Name the blood parasite species.
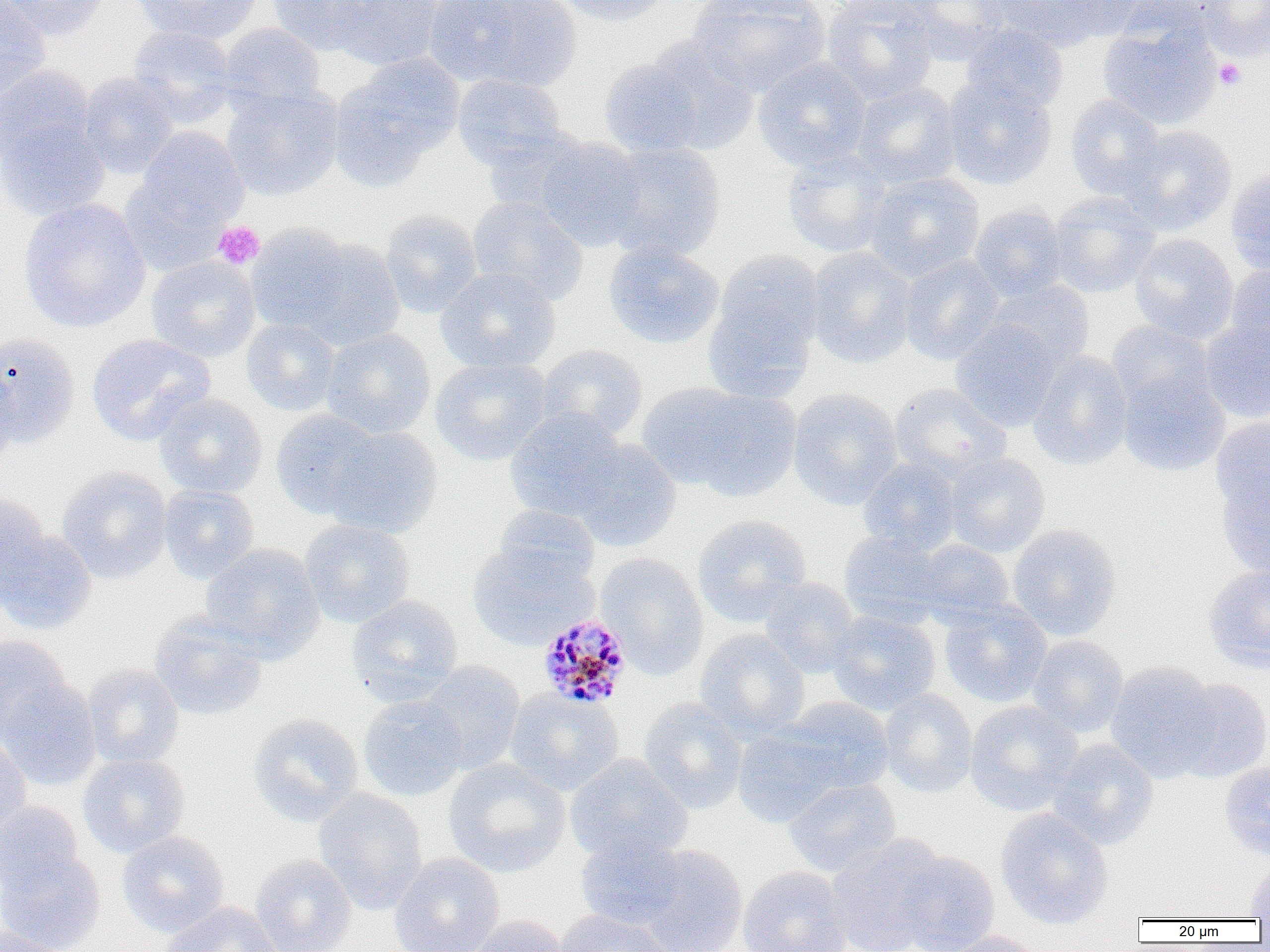

Plasmodium malariae.

Approximate bounding boxes as named x1/y1/x2/y2 corners in pixels. Uninfected red blood cell locations: (x1=0, y1=0, x2=50, y2=99), (x1=3, y1=0, x2=110, y2=39), (x1=134, y1=0, x2=263, y2=44), (x1=268, y1=0, x2=382, y2=55), (x1=328, y1=0, x2=444, y2=72), (x1=433, y1=0, x2=581, y2=92), (x1=553, y1=0, x2=671, y2=26), (x1=687, y1=0, x2=830, y2=96), (x1=822, y1=0, x2=940, y2=105), (x1=899, y1=0, x2=1014, y2=65), (x1=986, y1=0, x2=1127, y2=50), (x1=1044, y1=0, x2=1157, y2=40), (x1=1195, y1=0, x2=1270, y2=61), (x1=1099, y1=19, x2=1222, y2=130), (x1=217, y1=23, x2=327, y2=117), (x1=960, y1=24, x2=1068, y2=116), (x1=127, y1=26, x2=237, y2=129), (x1=643, y1=37, x2=759, y2=155), (x1=598, y1=56, x2=707, y2=157), (x1=752, y1=56, x2=872, y2=172), (x1=332, y1=58, x2=462, y2=186), (x1=0, y1=64, x2=95, y2=163), (x1=78, y1=72, x2=179, y2=179), (x1=453, y1=73, x2=567, y2=169), (x1=942, y1=77, x2=1058, y2=191), (x1=848, y1=82, x2=961, y2=188), (x1=221, y1=86, x2=344, y2=200), (x1=1065, y1=94, x2=1167, y2=201), (x1=0, y1=117, x2=110, y2=220), (x1=1118, y1=124, x2=1237, y2=235), (x1=135, y1=127, x2=250, y2=232), (x1=483, y1=128, x2=591, y2=220), (x1=534, y1=137, x2=646, y2=251), (x1=600, y1=141, x2=727, y2=262), (x1=782, y1=147, x2=896, y2=259), (x1=1225, y1=170, x2=1270, y2=275), (x1=864, y1=172, x2=985, y2=282), (x1=1047, y1=193, x2=1161, y2=297), (x1=467, y1=196, x2=588, y2=306), (x1=18, y1=198, x2=151, y2=333), (x1=969, y1=203, x2=1067, y2=301), (x1=381, y1=209, x2=482, y2=318), (x1=246, y1=223, x2=356, y2=335), (x1=1129, y1=233, x2=1239, y2=344), (x1=294, y1=237, x2=405, y2=350), (x1=603, y1=241, x2=724, y2=349), (x1=806, y1=246, x2=917, y2=369), (x1=703, y1=251, x2=824, y2=399), (x1=899, y1=254, x2=1005, y2=365), (x1=145, y1=256, x2=260, y2=362), (x1=1225, y1=263, x2=1270, y2=367), (x1=436, y1=267, x2=561, y2=374), (x1=986, y1=278, x2=1095, y2=372), (x1=242, y1=319, x2=341, y2=416), (x1=1201, y1=319, x2=1270, y2=423), (x1=950, y1=320, x2=1060, y2=432), (x1=1107, y1=321, x2=1217, y2=418), (x1=321, y1=328, x2=436, y2=440), (x1=0, y1=333, x2=80, y2=448), (x1=86, y1=333, x2=215, y2=445), (x1=536, y1=345, x2=648, y2=443), (x1=1028, y1=351, x2=1134, y2=471), (x1=430, y1=356, x2=552, y2=466), (x1=0, y1=364, x2=18, y2=470), (x1=1117, y1=369, x2=1231, y2=477), (x1=890, y1=383, x2=1011, y2=482), (x1=647, y1=385, x2=802, y2=500), (x1=787, y1=387, x2=903, y2=509), (x1=154, y1=392, x2=268, y2=499), (x1=503, y1=408, x2=627, y2=522), (x1=270, y1=409, x2=384, y2=520), (x1=1210, y1=417, x2=1270, y2=520), (x1=321, y1=425, x2=442, y2=538), (x1=568, y1=438, x2=682, y2=552), (x1=942, y1=453, x2=1051, y2=557), (x1=858, y1=458, x2=961, y2=556), (x1=56, y1=466, x2=172, y2=583), (x1=1215, y1=469, x2=1270, y2=577), (x1=159, y1=485, x2=259, y2=584), (x1=0, y1=495, x2=54, y2=601), (x1=492, y1=503, x2=600, y2=589), (x1=693, y1=513, x2=812, y2=627), (x1=299, y1=519, x2=416, y2=627), (x1=1006, y1=524, x2=1122, y2=641), (x1=0, y1=527, x2=97, y2=634), (x1=839, y1=530, x2=949, y2=627), (x1=910, y1=538, x2=1015, y2=627), (x1=467, y1=542, x2=596, y2=650), (x1=200, y1=544, x2=325, y2=661), (x1=595, y1=552, x2=709, y2=680), (x1=1204, y1=562, x2=1270, y2=672), (x1=759, y1=577, x2=861, y2=678), (x1=345, y1=595, x2=464, y2=707), (x1=939, y1=599, x2=1053, y2=708), (x1=825, y1=609, x2=942, y2=715), (x1=148, y1=610, x2=268, y2=721), (x1=694, y1=628, x2=810, y2=741), (x1=1027, y1=635, x2=1129, y2=738), (x1=0, y1=636, x2=73, y2=741), (x1=1105, y1=660, x2=1220, y2=782), (x1=416, y1=661, x2=525, y2=774), (x1=83, y1=662, x2=185, y2=769), (x1=1, y1=677, x2=101, y2=791), (x1=1167, y1=677, x2=1270, y2=782), (x1=504, y1=688, x2=625, y2=796), (x1=879, y1=688, x2=978, y2=798), (x1=358, y1=694, x2=468, y2=802), (x1=776, y1=697, x2=895, y2=796), (x1=638, y1=698, x2=748, y2=814), (x1=964, y1=700, x2=1084, y2=816), (x1=248, y1=712, x2=364, y2=827), (x1=731, y1=726, x2=842, y2=828), (x1=0, y1=732, x2=31, y2=839), (x1=1048, y1=739, x2=1159, y2=849), (x1=78, y1=753, x2=190, y2=857), (x1=565, y1=754, x2=692, y2=864), (x1=443, y1=757, x2=571, y2=878), (x1=1220, y1=760, x2=1270, y2=860), (x1=783, y1=778, x2=902, y2=877), (x1=313, y1=788, x2=428, y2=915), (x1=0, y1=802, x2=85, y2=896), (x1=995, y1=808, x2=1114, y2=929), (x1=117, y1=830, x2=229, y2=937), (x1=574, y1=835, x2=687, y2=929), (x1=825, y1=835, x2=949, y2=952), (x1=635, y1=844, x2=748, y2=952), (x1=0, y1=847, x2=106, y2=951), (x1=893, y1=849, x2=1000, y2=951), (x1=389, y1=853, x2=505, y2=952), (x1=250, y1=854, x2=356, y2=952), (x1=1246, y1=862, x2=1270, y2=919), (x1=737, y1=865, x2=853, y2=952), (x1=157, y1=901, x2=282, y2=952), (x1=554, y1=908, x2=676, y2=952), (x1=465, y1=914, x2=570, y2=952), (x1=0, y1=926, x2=69, y2=952), (x1=936, y1=930, x2=1044, y2=952). Platelet locations: (x1=1200, y1=2, x2=1269, y2=60), (x1=1214, y1=59, x2=1245, y2=90), (x1=213, y1=221, x2=264, y2=269). Plasmodium malariae-infected red blood cell locations: (x1=537, y1=612, x2=633, y2=710). Thin blood smear. Light microscopy. Image is 1270×952 pixels. One field of a larger specimen. Captured at 1000x magnification.